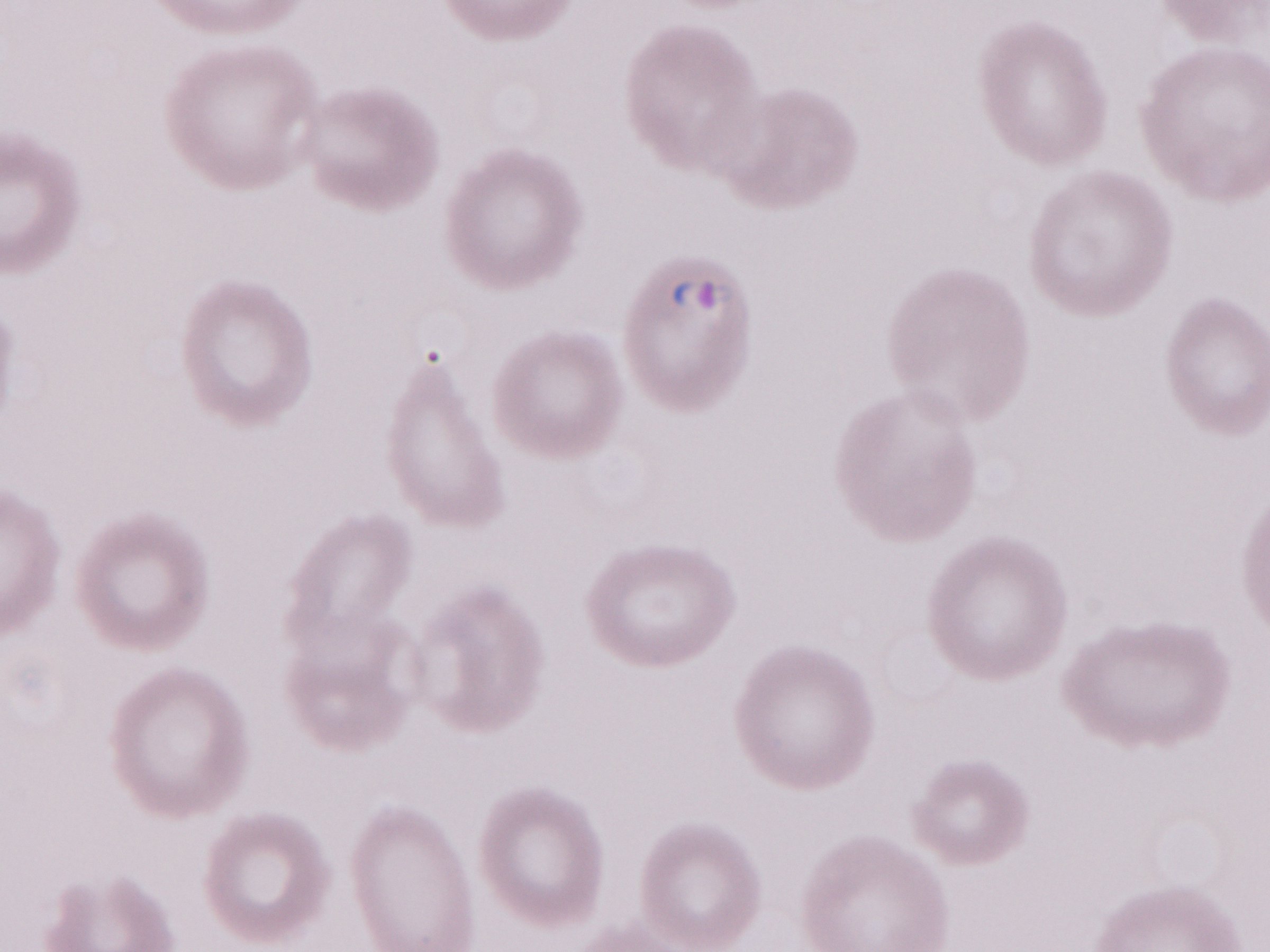
Malaria diagnosis (patient-level): positive. Single field of view. Thin peripheral-blood smear. May-Grünwald-Giemsa stain. Olympus BX43 microscope, Olympus DP73 camera. Magnification: 1,000x. Image is 1270×952 pixels.